Assess the morphology of the erythrocytes.
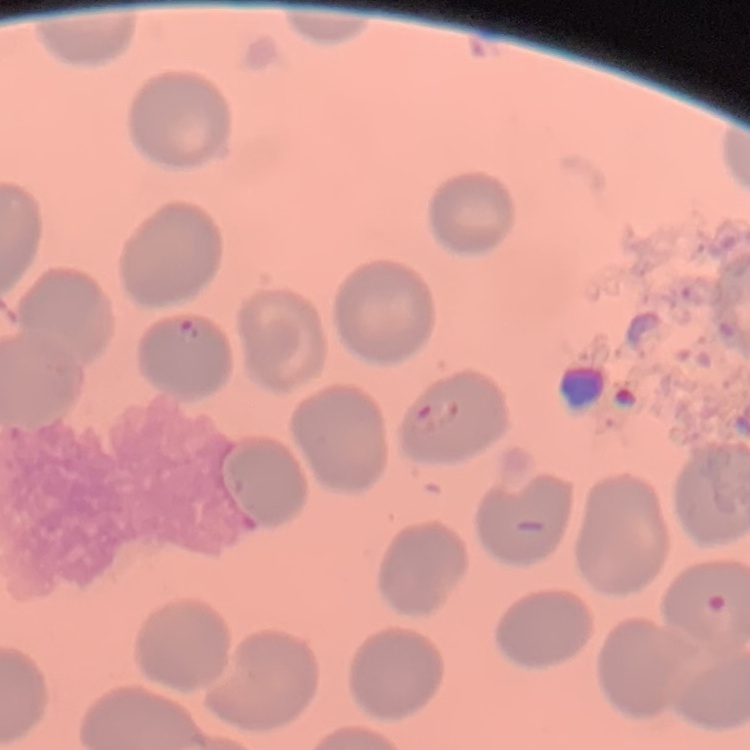

No rouleaux formation.

preparation: thin blood smear
image_type: one tile cut from a larger photomicrograph
stain: Field's or Giemsa